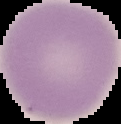
Summary:
  - Malaria status: uninfected
  - Image type: cell region segmented out of the field of view; surrounding area masked to black
  - Preparation: thin blood smear
  - Image size: 121×124 pixels